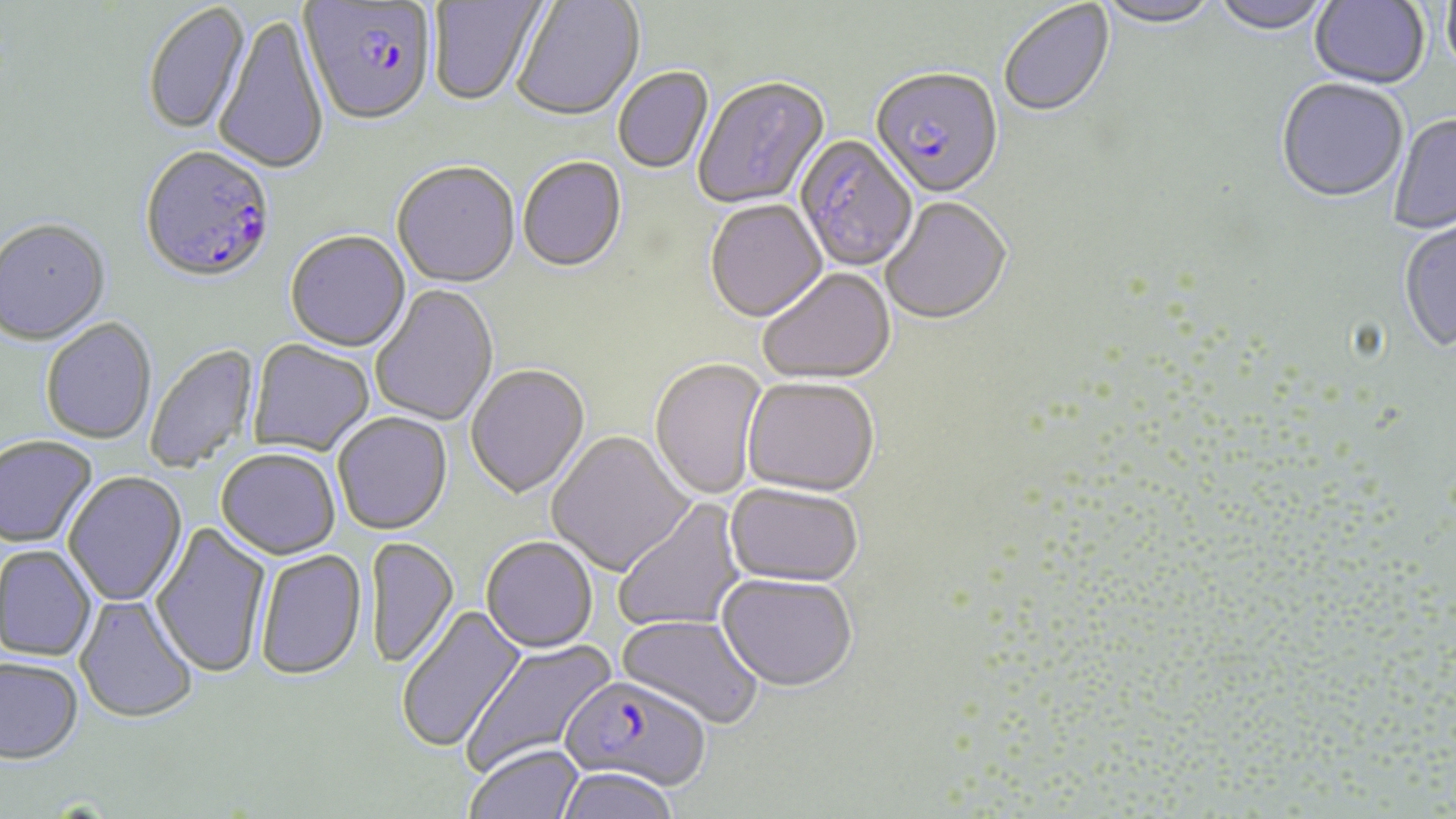
Approximate bounding boxes as (x1, y1, x2, y2) in pixels. Uninfected red blood cell locations: (429, 0, 547, 108), (513, 0, 645, 124), (1097, 0, 1221, 30), (1211, 0, 1332, 36), (1309, 0, 1430, 91), (1442, 1, 1456, 81), (143, 2, 251, 136), (999, 2, 1115, 120), (214, 14, 329, 176), (614, 68, 714, 174), (694, 78, 830, 212), (1276, 81, 1409, 205), (1389, 115, 1456, 235), (794, 135, 918, 274), (518, 159, 627, 275), (392, 164, 520, 291), (881, 197, 1013, 327), (705, 201, 828, 325), (0, 219, 111, 346), (1399, 219, 1456, 353), (285, 232, 411, 353), (758, 269, 896, 386), (370, 285, 500, 427), (40, 317, 158, 445), (248, 339, 374, 456), (144, 343, 261, 474), (649, 359, 768, 500), (465, 365, 591, 501), (741, 379, 879, 498), (332, 412, 453, 535), (547, 431, 695, 577), (0, 435, 98, 548), (216, 447, 341, 559), (63, 470, 188, 607), (725, 484, 864, 587), (613, 498, 748, 633), (151, 520, 272, 679), (367, 537, 459, 670), (481, 537, 598, 654), (1, 546, 98, 661), (254, 549, 368, 681), (716, 573, 858, 693), (74, 594, 199, 724), (395, 604, 528, 754), (615, 614, 763, 730), (460, 635, 617, 778), (0, 656, 83, 763), (464, 743, 585, 819), (555, 768, 681, 819). Plasmodium falciparum-infected red blood cell locations: (299, 2, 436, 130), (869, 71, 1004, 202), (139, 145, 277, 286), (560, 676, 711, 792). Slide-level diagnosis: Plasmodium falciparum. Thin blood smear. Captured at 1000x magnification. One field of a larger specimen. Light microscopy. Image is 1456×819 pixels. May-Grünwald-Giemsa-stained preparation.